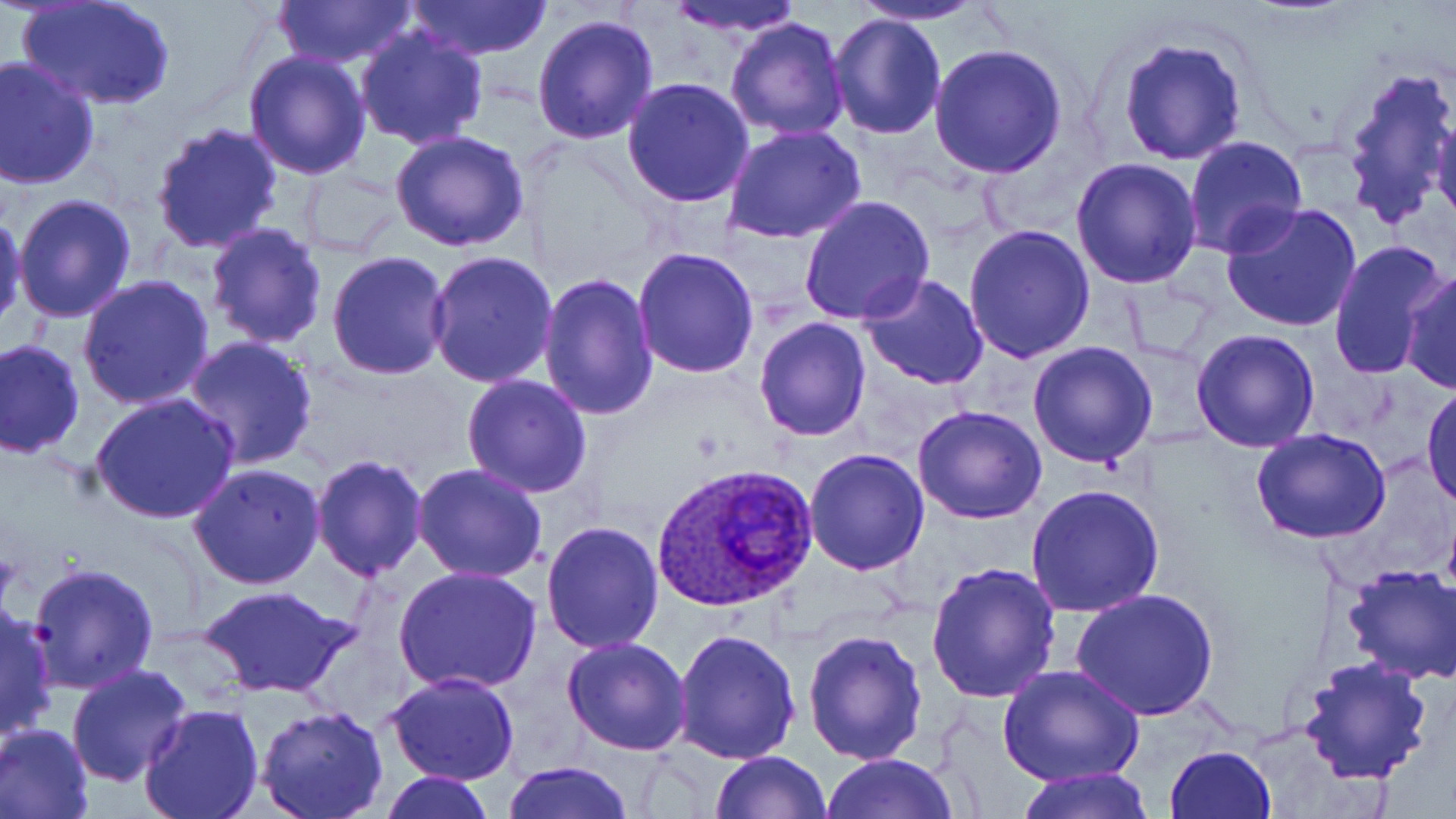
Summary:
  - Coordinate format: approximate bounding boxes as [x1, y1, x2, y2] in pixels
  - Plasmodium ovale-infected red blood cell locations: [654, 462, 818, 613]
  - Uninfected red blood cell locations: [271, 0, 419, 71], [406, 0, 554, 62], [665, 0, 811, 37], [847, 0, 992, 25], [19, 2, 173, 111], [828, 11, 946, 139], [530, 12, 659, 143], [723, 16, 850, 141], [355, 26, 490, 150], [1118, 37, 1247, 166], [929, 43, 1067, 178], [242, 49, 373, 178], [0, 57, 101, 190], [1337, 60, 1455, 234], [622, 77, 755, 209], [1431, 110, 1456, 230], [149, 120, 283, 252], [723, 126, 866, 244], [389, 129, 530, 253], [1184, 135, 1308, 256], [1071, 157, 1203, 289], [299, 167, 408, 257], [12, 192, 140, 324], [800, 195, 934, 324], [1220, 201, 1362, 334], [1, 211, 27, 331], [205, 223, 330, 351], [963, 224, 1096, 363], [1330, 239, 1452, 380], [632, 246, 762, 378], [327, 250, 453, 379], [426, 251, 559, 388], [867, 254, 1088, 380], [1400, 267, 1454, 396], [536, 272, 659, 420], [857, 272, 989, 390], [76, 274, 217, 411], [754, 318, 872, 441], [1191, 328, 1321, 453], [180, 336, 319, 471], [0, 339, 85, 459], [1027, 341, 1159, 468], [462, 373, 593, 497], [1422, 382, 1456, 511], [89, 392, 241, 525], [912, 405, 1047, 525], [1251, 429, 1394, 545], [803, 448, 930, 575], [309, 455, 429, 582], [188, 462, 328, 590], [411, 463, 552, 586], [1025, 483, 1166, 617], [541, 519, 667, 653], [28, 563, 160, 693], [924, 563, 1064, 705], [1341, 564, 1456, 685], [392, 566, 543, 696], [196, 583, 355, 698], [1071, 589, 1217, 720], [0, 603, 57, 743], [672, 626, 802, 764], [802, 627, 928, 764], [563, 635, 692, 755], [1298, 656, 1434, 786], [67, 663, 195, 787], [1000, 666, 1142, 788], [384, 671, 520, 785], [139, 704, 265, 819], [254, 706, 388, 819], [1, 722, 94, 819], [1163, 745, 1276, 819], [709, 750, 833, 818], [822, 753, 958, 819], [500, 761, 635, 819], [1009, 770, 1155, 819], [379, 772, 494, 818]
  - Slide-level diagnosis: Plasmodium ovale
  - Stain: May-Grünwald-Giemsa
  - Field of view: one of a larger specimen
  - Magnification: 1000x
  - Preparation: thin blood film
  - Image size: 1456×819 pixels
  - Modality: light microscopy